Locate and identify every blood parasite.
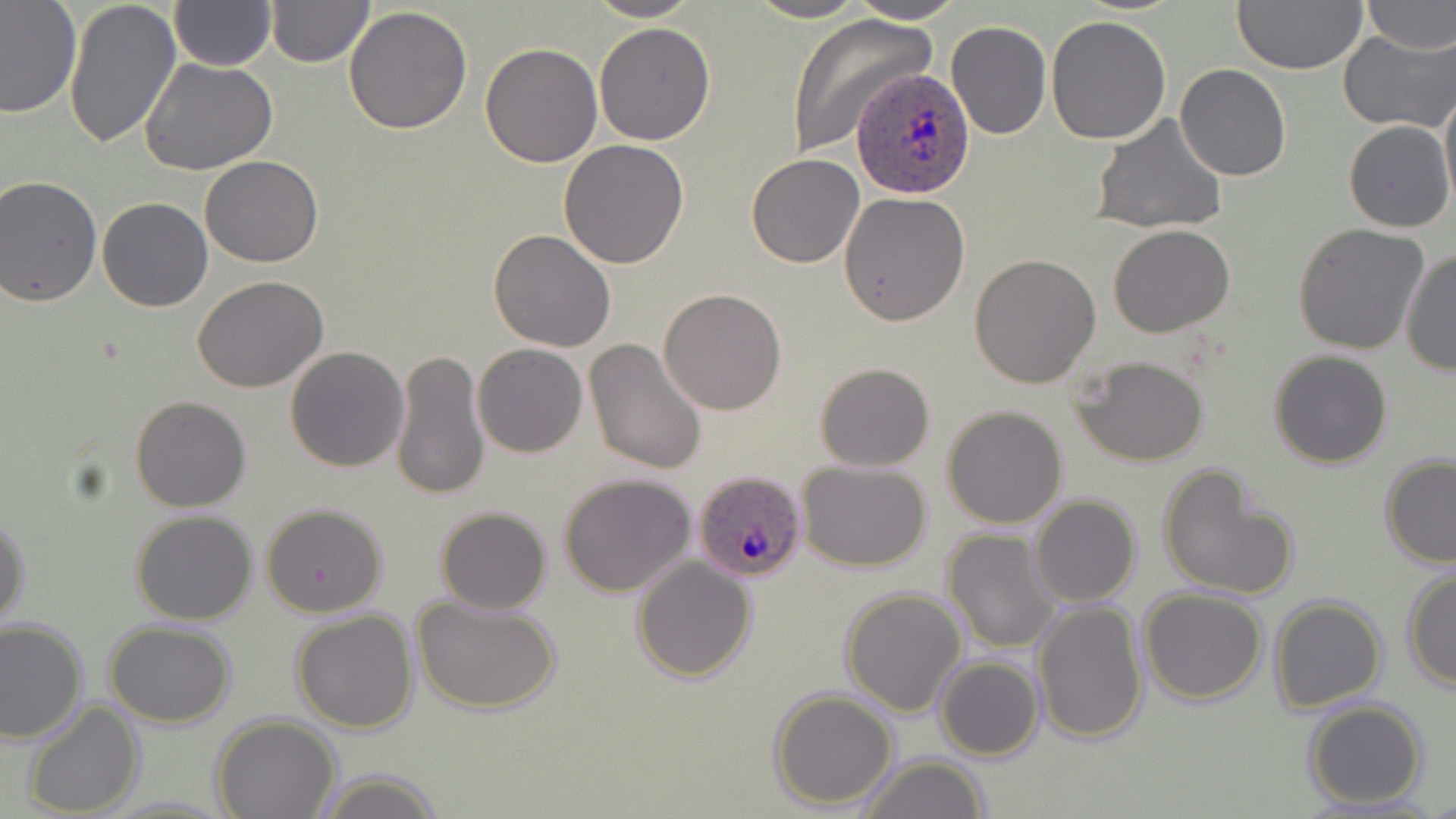
Approximate bounding boxes as (x1, y1, x2, y2) in pixels.
Plasmodium ovale-infected red blood cells: (855, 67, 977, 200), (692, 470, 809, 583).
No Plasmodium falciparum, Plasmodium malariae, Plasmodium vivax, Babesia divergens, or Trypanosoma brucei observed.

Uninfected red blood cell locations: (62, 0, 181, 148), (584, 0, 704, 22), (745, 0, 871, 23), (847, 0, 968, 23), (1231, 0, 1369, 76), (1361, 0, 1455, 53), (169, 1, 277, 71), (0, 2, 80, 117), (265, 2, 375, 68), (343, 7, 473, 133), (784, 12, 938, 157), (1046, 16, 1170, 144), (593, 21, 717, 146), (946, 21, 1051, 139), (1339, 30, 1455, 132), (480, 43, 603, 167), (140, 56, 278, 175), (1175, 65, 1291, 182), (1439, 82, 1456, 214), (1090, 115, 1229, 235), (1344, 120, 1453, 233), (558, 139, 690, 269), (746, 154, 864, 269), (200, 156, 323, 268), (0, 174, 103, 307), (838, 191, 969, 326), (98, 197, 212, 312), (1293, 223, 1429, 357), (1108, 225, 1235, 337), (489, 230, 617, 352), (1400, 249, 1455, 377), (969, 253, 1101, 387), (194, 274, 329, 391), (659, 288, 787, 413), (584, 337, 708, 474), (472, 344, 588, 458), (284, 346, 410, 471), (391, 349, 490, 503), (1268, 349, 1392, 468), (1071, 354, 1210, 467), (814, 363, 935, 472), (130, 395, 252, 512), (941, 406, 1068, 528), (1379, 454, 1456, 568), (796, 461, 931, 570), (1157, 464, 1300, 602), (558, 472, 698, 596), (1029, 495, 1141, 608), (260, 503, 389, 617), (435, 507, 551, 615), (130, 511, 257, 625), (0, 512, 31, 635), (940, 528, 1062, 653), (632, 555, 756, 681), (1401, 568, 1456, 692), (1137, 587, 1268, 705), (840, 588, 968, 716), (1268, 595, 1388, 714), (415, 596, 560, 716), (1029, 599, 1147, 746), (291, 609, 420, 734), (0, 619, 88, 745), (103, 621, 236, 727), (934, 655, 1044, 762), (768, 688, 899, 810), (1302, 698, 1430, 809), (22, 699, 145, 818), (212, 715, 341, 819), (852, 753, 995, 819), (310, 770, 450, 819). Slide-level diagnosis: Plasmodium ovale. Single field of view. Thin blood film. Light microscopy. 1000x magnification. Image is 1456×819 pixels. May-Grünwald-Giemsa stain.